Evaluate for parasitized red blood cells.
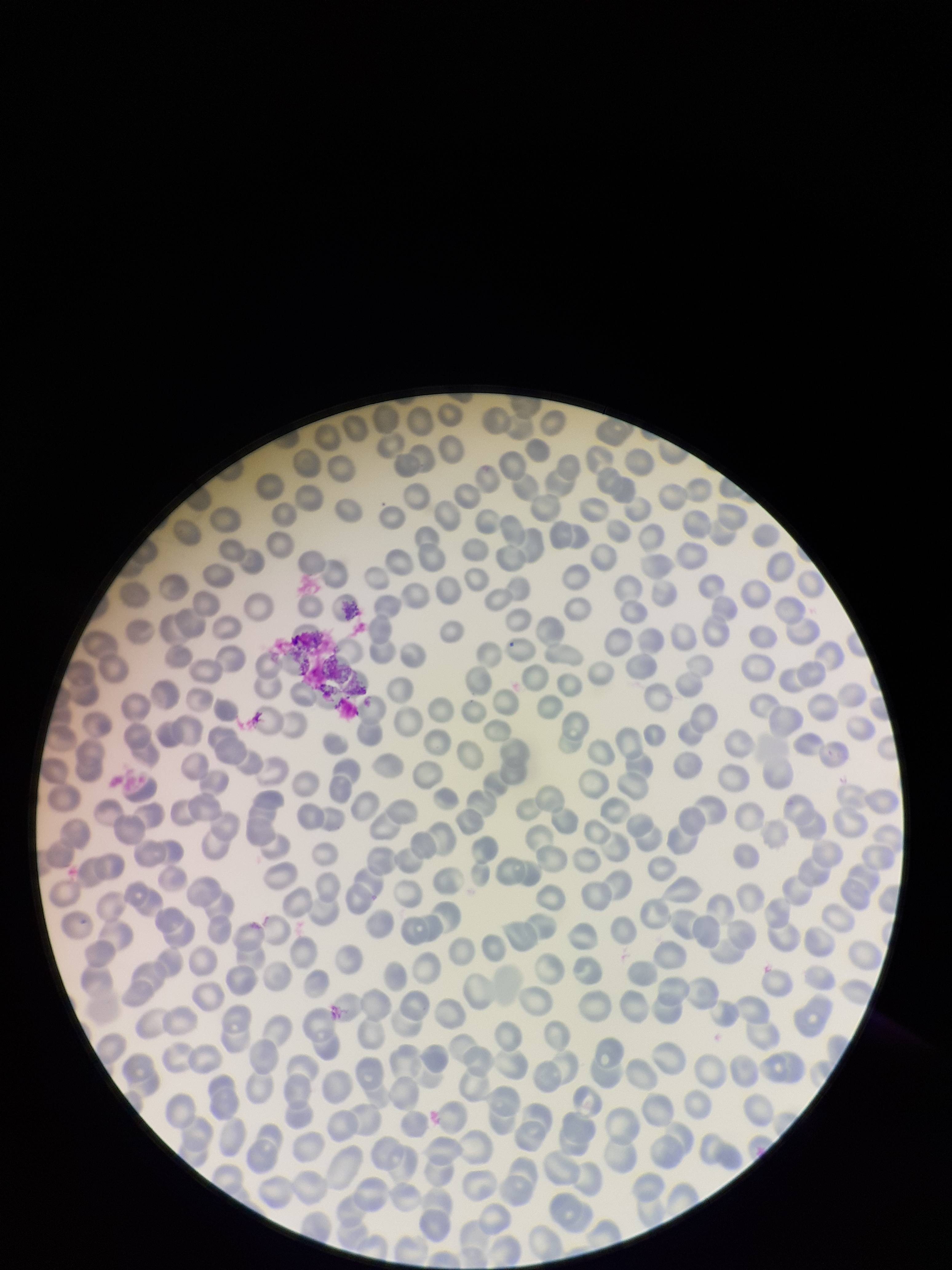
None seen.

Summary:
  - Preparation: thin
  - Stain: Giemsa
  - Capture: smartphone photograph through the microscope eyepiece
  - Patient malaria status: negative
  - Parasitized red blood cell count: 0
  - Red blood cell count: 272
  - Image size: 952×1270 pixels
  - Field of view: one from this slide